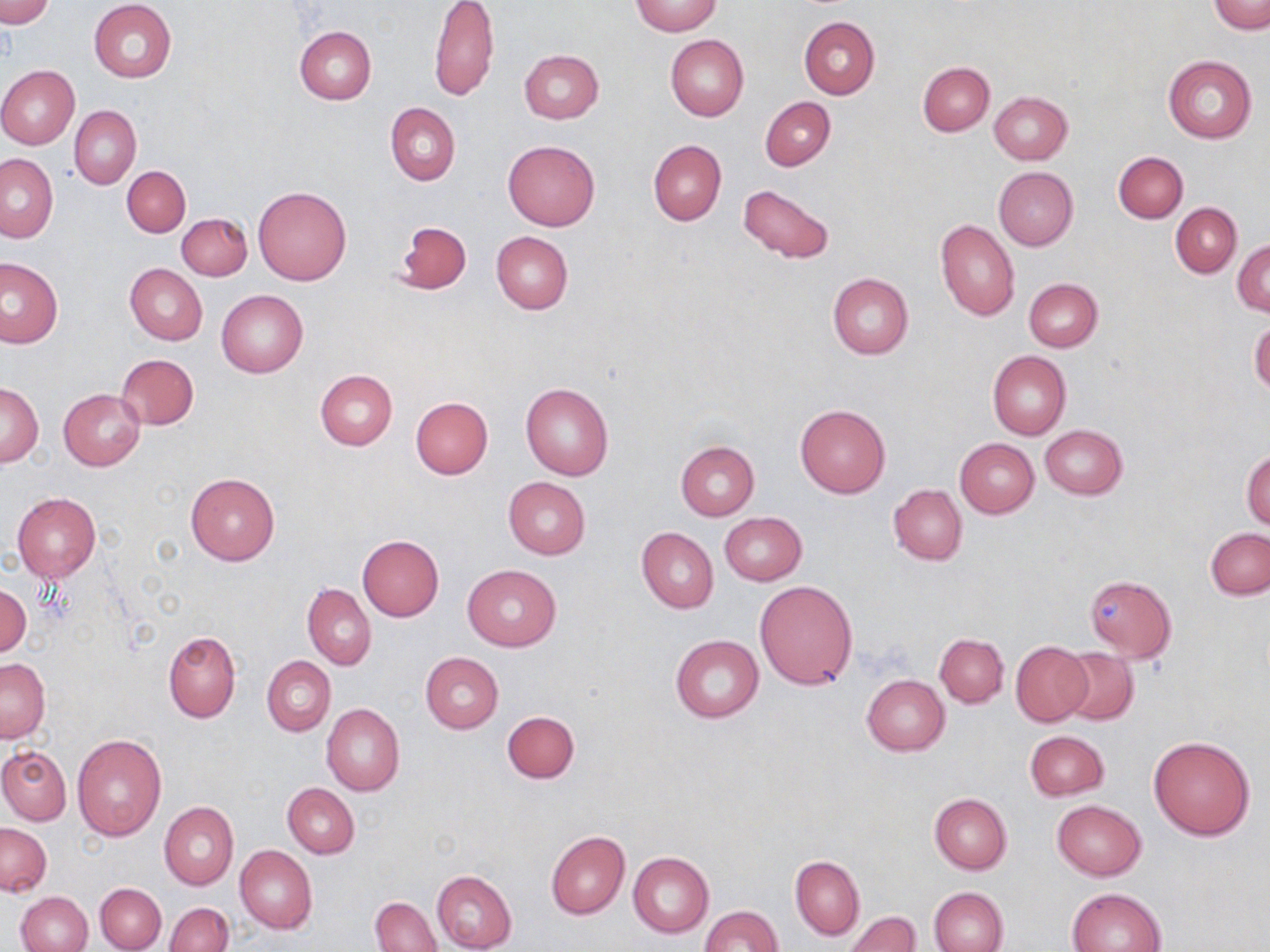

Summary:
  - Coordinate format: approximate bounding boxes as (x1,y1)-(x2,y2) corner pairs in pixels
  - Uninfected red blood cell locations: (0,0)-(54,27), (89,1)-(177,82), (429,1)-(500,100), (631,1)-(722,36), (1209,1)-(1269,33), (798,17)-(879,99), (295,25)-(377,103), (666,35)-(748,121), (518,49)-(603,123), (1163,54)-(1257,144), (918,62)-(994,136), (0,66)-(79,149), (989,90)-(1073,164), (760,96)-(835,171), (385,102)-(460,186), (70,105)-(141,189), (503,140)-(600,231), (647,140)-(726,226), (1114,151)-(1187,222), (0,153)-(58,242), (122,166)-(190,237), (993,167)-(1077,251), (737,183)-(835,264), (253,184)-(352,285), (1171,203)-(1242,278), (177,213)-(252,280), (392,219)-(472,295), (936,219)-(1020,322), (491,232)-(573,314), (1234,241)-(1269,316), (0,258)-(63,348), (125,264)-(207,345), (827,273)-(914,359), (1024,277)-(1102,351), (216,290)-(308,378), (1249,319)-(1270,395), (987,351)-(1071,439), (117,354)-(199,429), (315,369)-(397,450), (2,381)-(43,467), (520,382)-(615,480), (59,389)-(145,471), (410,396)-(493,479), (795,403)-(891,498), (1040,425)-(1126,500), (955,438)-(1038,518), (676,441)-(759,519), (1241,448)-(1270,530), (186,472)-(280,565), (503,476)-(591,559), (888,484)-(968,566), (12,492)-(102,581), (720,512)-(807,586), (636,527)-(718,612), (1206,527)-(1270,599), (357,535)-(444,621), (462,563)-(561,652), (1086,575)-(1174,662), (755,580)-(857,690), (0,584)-(30,659), (302,584)-(376,669), (163,631)-(240,722), (671,634)-(764,722), (935,634)-(1008,707), (1010,642)-(1092,726), (1058,647)-(1138,725), (421,652)-(504,733), (262,656)-(334,735), (1,659)-(50,743), (862,674)-(950,755), (321,704)-(404,796), (502,710)-(578,784), (1025,730)-(1108,800), (72,733)-(167,840), (1148,736)-(1256,841), (0,747)-(71,824), (282,783)-(359,858), (929,793)-(1012,874), (1052,800)-(1146,880), (160,802)-(238,889), (1,823)-(51,897), (546,831)-(630,919), (235,844)-(317,934), (629,851)-(713,937), (790,856)-(864,940), (432,870)-(517,952), (95,882)-(166,951), (930,886)-(1009,952), (1067,887)-(1166,952), (15,891)-(92,952), (371,895)-(441,951), (165,902)-(233,952), (700,906)-(782,952), (847,911)-(921,952)
  - Slide-level diagnosis: negative for blood parasites
  - Image size: 1270×952 pixels
  - Field of view: one of a larger specimen
  - Magnification: 1000x
  - Preparation: thin blood smear
  - Modality: optical microscopy
  - Stain: May-Grünwald-Giemsa